Point out each Plasmodium parasite.
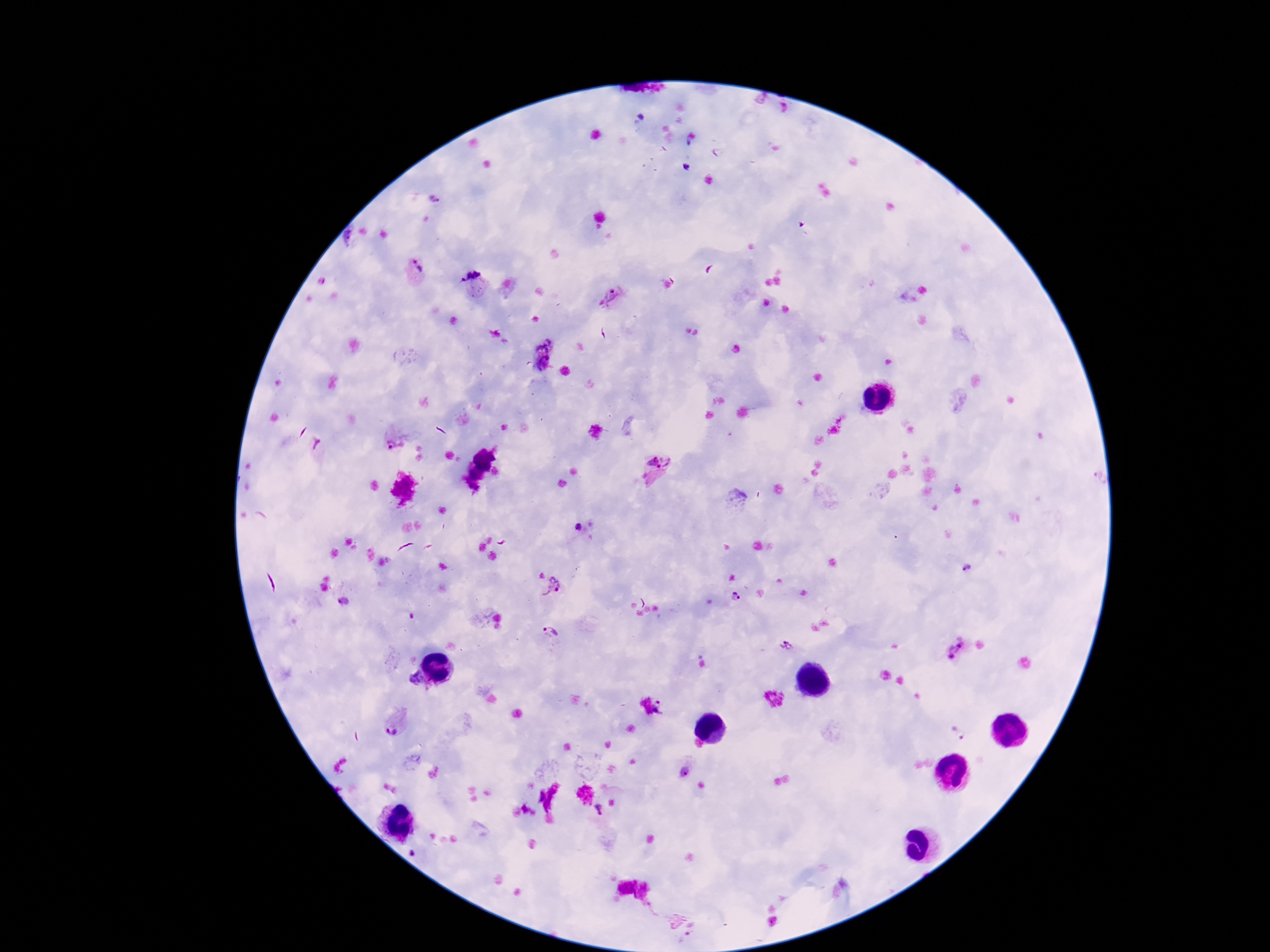

Approximate centers as (x, y) in pixels.
Plasmodium parasites: (686, 167), (433, 200), (416, 269), (470, 274), (614, 298), (542, 353), (390, 442), (656, 467), (579, 527), (968, 570), (553, 586), (735, 599), (344, 602), (549, 632), (787, 646), (954, 649), (413, 678), (665, 706), (395, 725), (959, 732), (684, 772), (599, 811).

field of view = one from this slide
capture = smartphone camera through the microscope eyepiece
patient malaria status = positive
stain = Giemsa
magnification = 100x
image size = 1270×952 pixels
preparation = thick blood smear